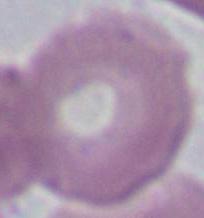

Micrograph. Captured at 1000x magnification. An erythrocyte is shown.